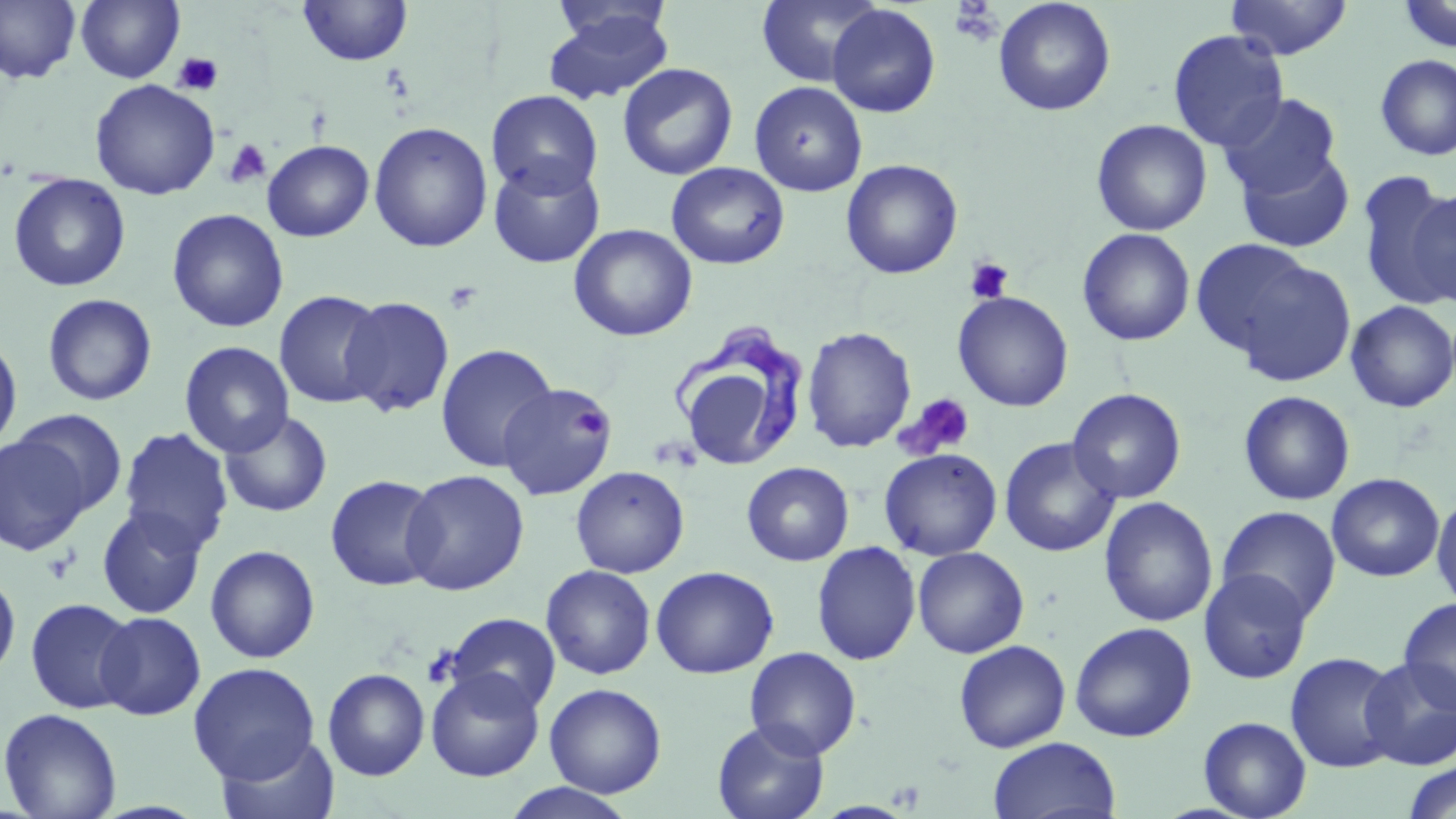
slide-level diagnosis = Trypanosoma brucei
image size = 1456×819 pixels
magnification = 1000x
preparation = thin blood smear
Trypanosoma brucei locations = approximate bounding boxes as (x1,y1)-(x2,y2) corner pairs in pixels: (671,328)-(811,473)
field of view = one of a larger specimen
platelet locations = approximate bounding boxes as (x1,y1)-(x2,y2) corner pairs in pixels: (948,3)-(1003,47), (172,52)-(224,96), (223,138)-(272,188), (965,257)-(1015,304), (443,280)-(483,316), (899,393)-(975,458), (575,406)-(612,441), (43,551)-(79,584)
stain = May-Grünwald-Giemsa
modality = optical microscopy
uninfected red blood cell locations = approximate bounding boxes as (x1,y1)-(x2,y2) corner pairs in pixels: (0,0)-(81,85), (75,0)-(184,83), (756,0)-(884,87), (993,0)-(1116,117), (1225,0)-(1353,60), (1396,0)-(1456,54), (297,1)-(414,67), (549,1)-(675,52), (827,4)-(941,118), (541,10)-(674,106), (1168,29)-(1288,151), (1374,54)-(1456,162), (617,62)-(738,180), (90,79)-(221,200), (749,81)-(868,197), (487,90)-(603,198), (1219,93)-(1342,199), (1091,119)-(1212,236), (369,122)-(493,253), (262,140)-(374,242), (1236,147)-(1355,254), (488,158)-(606,269), (841,159)-(963,279), (666,162)-(790,269), (1355,172)-(1454,309), (7,173)-(131,292), (1406,187)-(1456,307), (167,208)-(289,333), (568,224)-(698,341), (1077,227)-(1196,346), (1189,238)-(1318,358), (1230,258)-(1357,388), (274,289)-(386,408), (952,291)-(1073,412), (42,293)-(158,406), (339,296)-(455,418), (1345,300)-(1456,413), (802,326)-(917,453), (0,334)-(22,453), (179,341)-(294,457), (436,344)-(558,473), (686,373)-(783,466), (496,382)-(613,502), (1066,388)-(1187,504), (1239,390)-(1355,506), (14,409)-(128,517), (219,410)-(333,518), (118,428)-(234,555), (0,435)-(90,555), (999,437)-(1121,557), (879,447)-(1003,560), (741,462)-(854,566), (570,465)-(690,578), (401,469)-(530,596), (1326,473)-(1445,582), (325,475)-(444,592), (1431,492)-(1456,613), (1098,496)-(1218,627), (96,506)-(208,619), (1216,506)-(1341,623), (812,541)-(921,666), (205,545)-(321,664), (912,547)-(1029,658), (540,564)-(656,680), (650,565)-(779,679), (1198,568)-(1313,684), (0,570)-(21,683), (25,597)-(138,715), (1397,597)-(1456,714), (95,611)-(206,720), (444,612)-(561,716), (1069,622)-(1197,742), (953,639)-(1071,753), (744,646)-(862,759), (1285,652)-(1403,773), (1359,656)-(1456,771), (188,662)-(320,783), (426,667)-(544,781), (323,668)-(430,780), (426,675)-(663,790), (544,683)-(667,798), (0,707)-(123,819), (1198,716)-(1312,818), (712,720)-(830,819), (215,733)-(340,819), (987,737)-(1122,819), (1400,761)-(1456,819), (502,783)-(639,819)